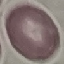

Summary:
  - Malaria status: uninfected
  - Capture: smartphone through the microscope eyepiece
  - Image type: automatically extracted cell patch, resized to 64 × 64 pixels
  - Stain: Giemsa
  - Preparation: thin blood film